Outline every parasitised red blood cell, every trophozoite, every gametocyte, every leukocyte, and every artifact (platelet-like body, stain precipitate, or debris).
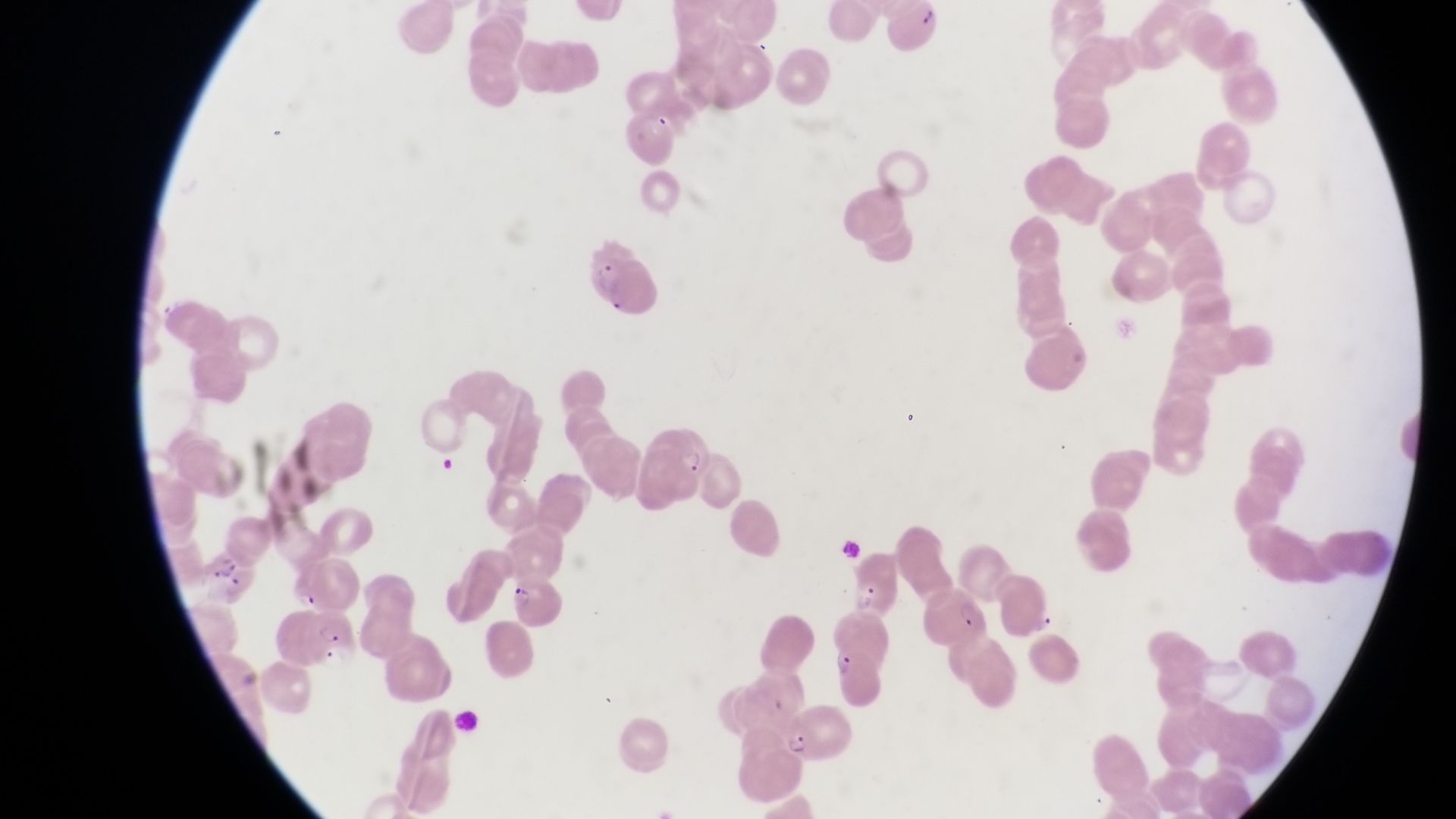
Approximate bounding boxes as [left, top, right, bottom] in pixels.
Parasitised red blood cells: [588, 243, 660, 317], [198, 547, 256, 602], [848, 552, 904, 621], [505, 574, 564, 629], [928, 582, 986, 642], [303, 607, 358, 673], [825, 642, 885, 714], [777, 704, 856, 765].
Trophozoites: [1033, 613, 1056, 640].
No leukocytes observed.
Artifacts (platelet-like body, stain precipitate, or debris): [835, 534, 861, 564].

Thin blood film. One field of view. Sample from Uganda. At a magnification of 1000x. Image is 1456×819 pixels. Photographed through the eyepiece of an Olympus CX-23 microscope with a smartphone camera.